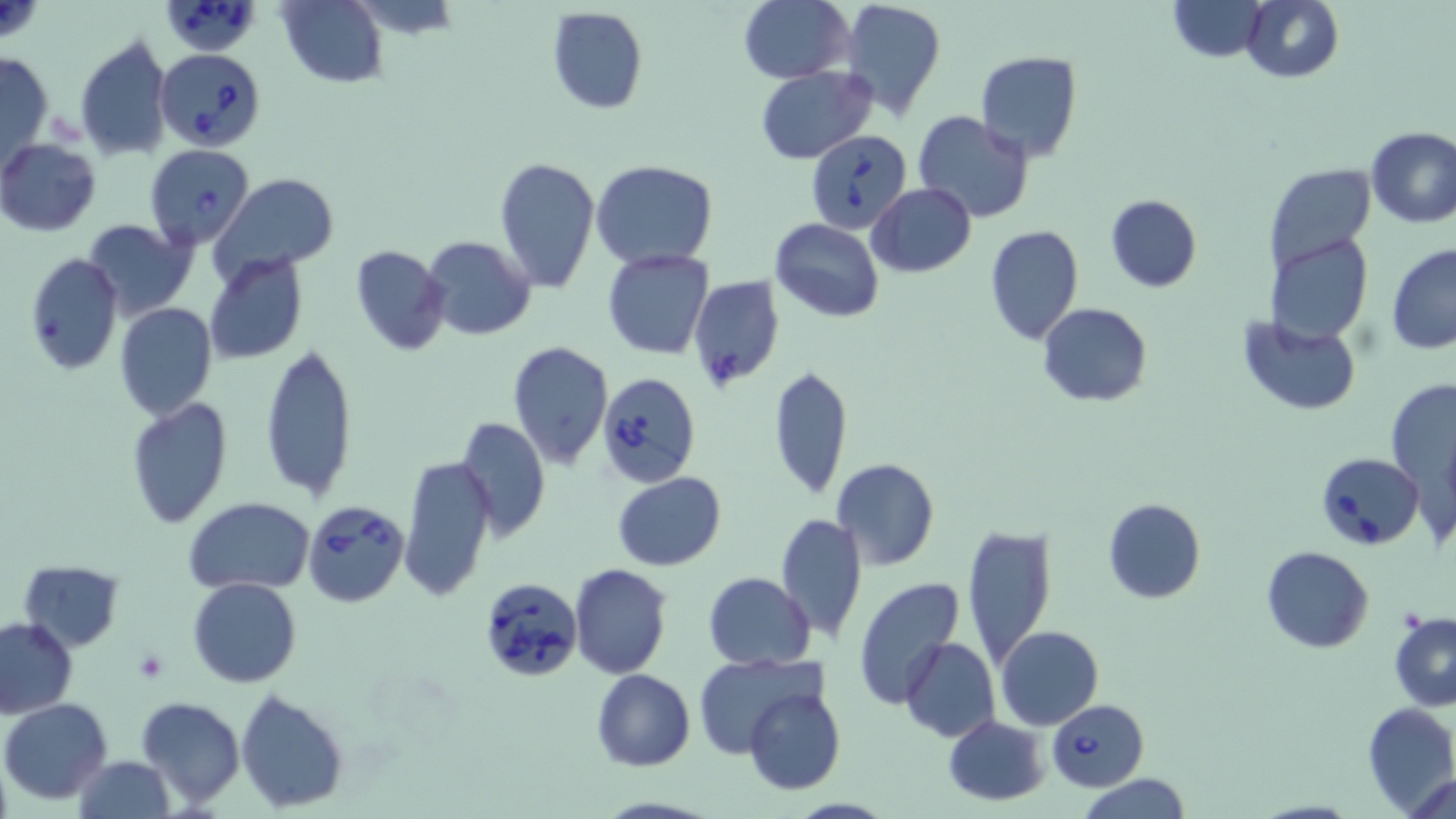

Approximate bounding boxes as [x1, y1, x2, y2] in pixels. Uninfected red blood cell locations: [281, 0, 386, 87], [738, 0, 853, 83], [840, 0, 946, 120], [1167, 0, 1266, 61], [1240, 0, 1343, 83], [545, 6, 648, 114], [74, 34, 173, 162], [0, 48, 53, 171], [975, 51, 1082, 160], [756, 66, 874, 164], [912, 111, 1036, 223], [1365, 127, 1456, 228], [0, 139, 101, 235], [495, 155, 601, 292], [591, 160, 717, 270], [1263, 160, 1376, 272], [212, 174, 339, 280], [866, 183, 976, 277], [1104, 193, 1202, 292], [771, 218, 884, 321], [80, 219, 197, 319], [985, 226, 1084, 346], [1267, 233, 1373, 346], [421, 235, 539, 340], [1386, 243, 1456, 354], [349, 244, 451, 358], [602, 250, 713, 359], [23, 252, 125, 376], [205, 252, 309, 366], [688, 275, 784, 392], [1037, 302, 1152, 407], [116, 303, 219, 420], [1238, 317, 1363, 417], [260, 342, 358, 502], [507, 342, 613, 468], [768, 364, 853, 501], [1385, 377, 1456, 495], [124, 397, 233, 529], [454, 415, 550, 541], [399, 453, 496, 603], [832, 458, 939, 570], [612, 472, 726, 570], [795, 490, 918, 618], [183, 496, 315, 596], [1102, 498, 1206, 604], [775, 511, 868, 645], [962, 523, 1055, 666], [1262, 546, 1373, 653], [17, 559, 125, 652], [571, 564, 673, 679], [703, 572, 815, 671], [852, 577, 965, 709], [188, 578, 302, 688], [1390, 615, 1456, 711], [0, 616, 78, 719], [996, 626, 1105, 730], [901, 636, 1000, 742], [692, 655, 822, 760], [591, 667, 694, 771], [743, 685, 847, 796], [236, 688, 349, 811], [136, 696, 244, 809], [2, 697, 112, 804], [1362, 704, 1455, 814], [942, 716, 1050, 805], [73, 754, 175, 819], [1410, 771, 1455, 819], [1080, 773, 1189, 819]. Platelet locations: [133, 648, 168, 684]. Babesia divergens-infected red blood cell locations: [160, 1, 265, 57], [157, 48, 265, 149], [808, 129, 911, 232], [145, 144, 255, 249], [595, 371, 701, 488], [1318, 450, 1427, 551], [303, 500, 410, 608], [478, 578, 584, 682], [1045, 698, 1148, 791]. Slide-level diagnosis: Babesia divergens. Image is 1456×819 pixels. Light microscopy. Thin blood smear. May-Grünwald-Giemsa-stained preparation. One field of a larger specimen. 1000x magnification.